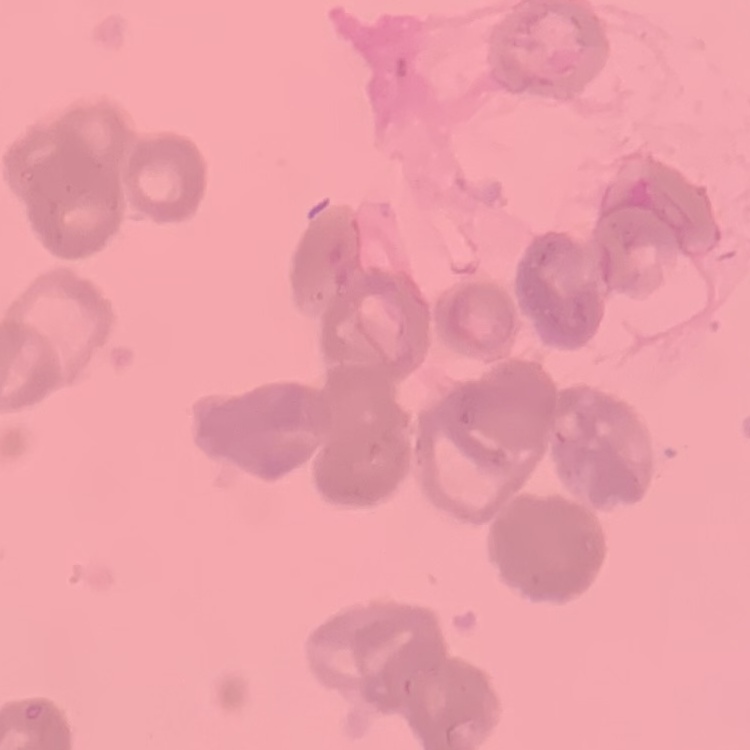

{
  "erythrocyte_morphology": "rouleaux formation",
  "stain": "Field's or Giemsa",
  "image_type": "one tile cut from a larger photomicrograph",
  "preparation": "thin blood smear"
}